Report the malaria status of this cell.
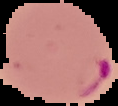

Parasitized.

image_type: cell region segmented out of the field of view; surrounding area masked to black
preparation: thin blood smear
image_size: 118×106 pixels